Assess for malaria.
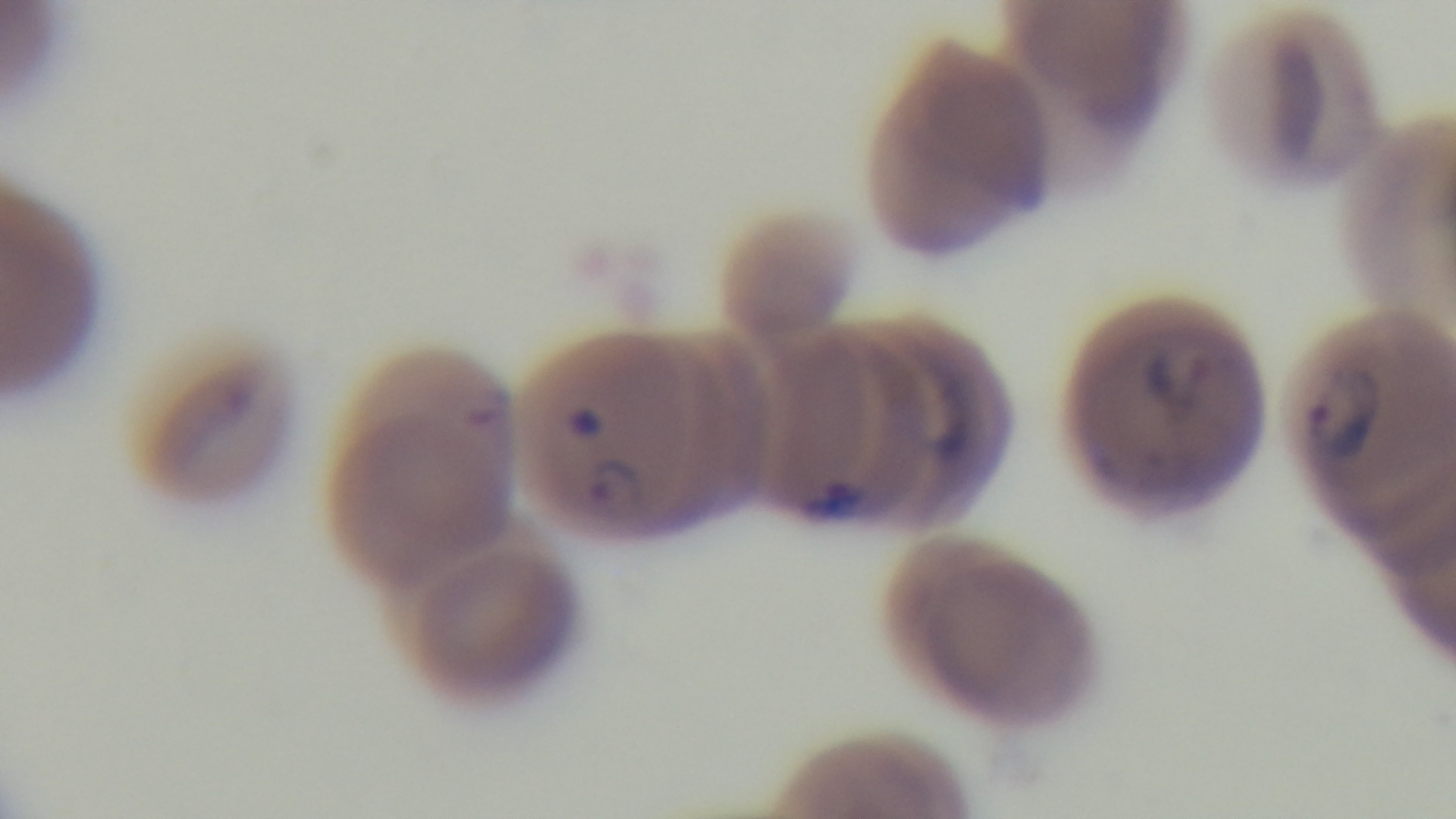
Infected.

{
  "stain": "Giemsa",
  "objective": "100x oil immersion",
  "preparation": "thin smear",
  "capture": "mounted 4K digital camera",
  "field_of_view": "one from the slide",
  "modality": "light microscopy"
}